Identify the cell.
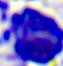
This is a leukocyte.

400x magnification. Micrograph.